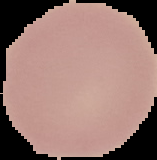

image_type: segmented cell region with the area outside set to black
malaria_status: uninfected
image_size: 157×160 pixels
preparation: thin blood smear